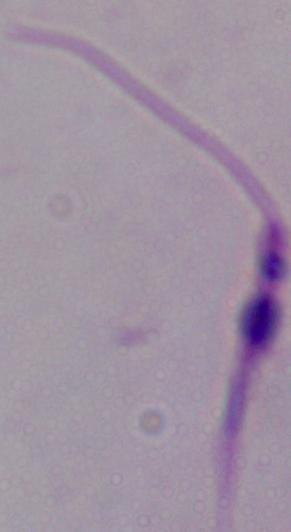
Captured at 1000x magnification. Photomicrograph. A Leishmania parasite is seen.